Describe the morphology of the red blood cells.
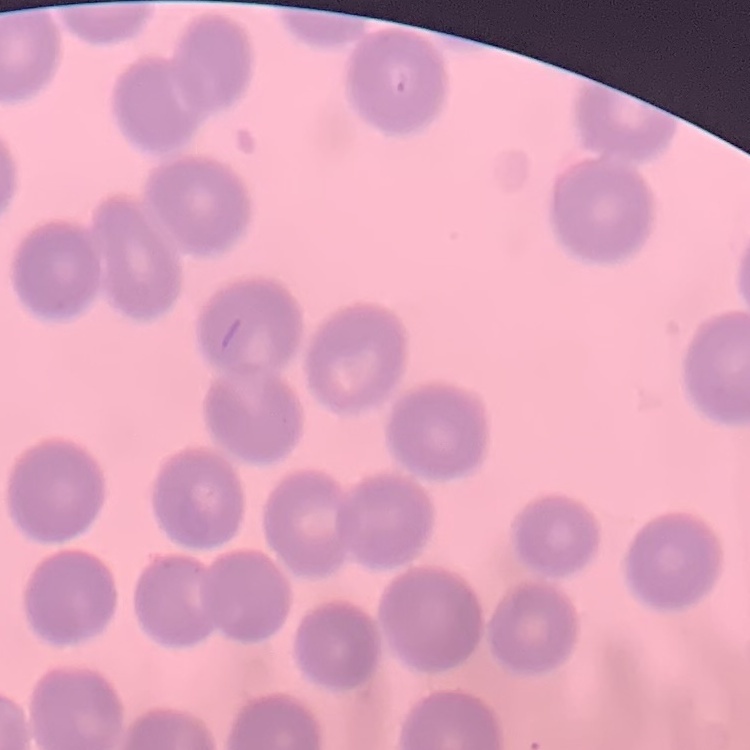

They show no rouleaux formation.

preparation = thin blood smear
image type = square crop of a larger photomicrograph
stain = Field's or Giemsa